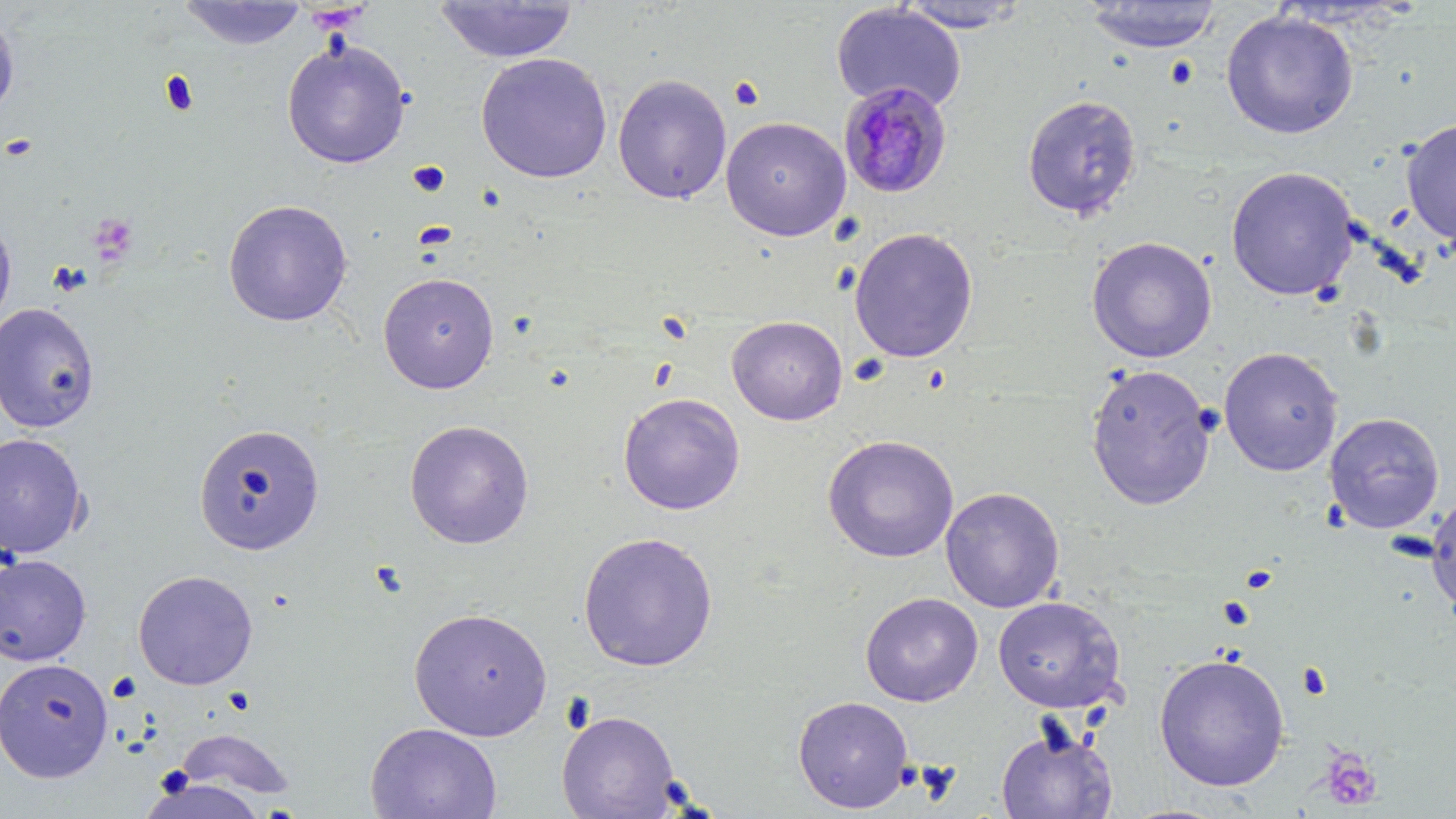
Approximate bounding boxes as named x1/y1/x2/y2 corners in pixels. Uninfected red blood cell locations: (x1=178, y1=1, x2=308, y2=50), (x1=434, y1=1, x2=579, y2=63), (x1=894, y1=1, x2=1033, y2=32), (x1=1082, y1=1, x2=1222, y2=53), (x1=831, y1=2, x2=967, y2=113), (x1=0, y1=7, x2=20, y2=121), (x1=1220, y1=10, x2=1358, y2=139), (x1=281, y1=39, x2=410, y2=169), (x1=476, y1=53, x2=613, y2=183), (x1=612, y1=74, x2=732, y2=205), (x1=1021, y1=93, x2=1142, y2=221), (x1=720, y1=116, x2=852, y2=242), (x1=1400, y1=117, x2=1456, y2=246), (x1=1225, y1=166, x2=1359, y2=301), (x1=222, y1=199, x2=353, y2=327), (x1=0, y1=215, x2=17, y2=333), (x1=849, y1=227, x2=979, y2=363), (x1=1086, y1=236, x2=1217, y2=363), (x1=377, y1=271, x2=500, y2=394), (x1=0, y1=302, x2=101, y2=433), (x1=726, y1=315, x2=848, y2=425), (x1=1218, y1=346, x2=1344, y2=476), (x1=1085, y1=363, x2=1216, y2=511), (x1=617, y1=392, x2=745, y2=515), (x1=1324, y1=412, x2=1445, y2=534), (x1=404, y1=420, x2=535, y2=549), (x1=194, y1=423, x2=325, y2=555), (x1=0, y1=432, x2=90, y2=559), (x1=822, y1=434, x2=960, y2=563), (x1=940, y1=487, x2=1065, y2=613), (x1=1426, y1=491, x2=1456, y2=622), (x1=578, y1=532, x2=720, y2=672), (x1=0, y1=554, x2=92, y2=666), (x1=132, y1=569, x2=259, y2=690), (x1=860, y1=592, x2=983, y2=706), (x1=992, y1=596, x2=1126, y2=713), (x1=408, y1=607, x2=553, y2=741), (x1=1153, y1=653, x2=1290, y2=791), (x1=0, y1=658, x2=114, y2=783), (x1=793, y1=695, x2=914, y2=813), (x1=556, y1=710, x2=681, y2=819), (x1=365, y1=722, x2=503, y2=819), (x1=996, y1=726, x2=1117, y2=819), (x1=175, y1=727, x2=296, y2=799). Platelet locations: (x1=159, y1=70, x2=200, y2=116), (x1=728, y1=76, x2=765, y2=110), (x1=2, y1=133, x2=39, y2=161), (x1=407, y1=161, x2=450, y2=198), (x1=90, y1=213, x2=139, y2=263), (x1=49, y1=262, x2=93, y2=296), (x1=1239, y1=565, x2=1277, y2=594), (x1=1218, y1=596, x2=1254, y2=629), (x1=1296, y1=662, x2=1332, y2=700), (x1=1320, y1=748, x2=1384, y2=811). Plasmodium malariae-infected red blood cell locations: (x1=837, y1=81, x2=953, y2=200). Slide-level diagnosis: Plasmodium malariae. One field of a larger specimen. Thin blood film. Optical microscopy. Captured at 1000x magnification. Image is 1456×819 pixels. May-Grünwald-Giemsa stain.